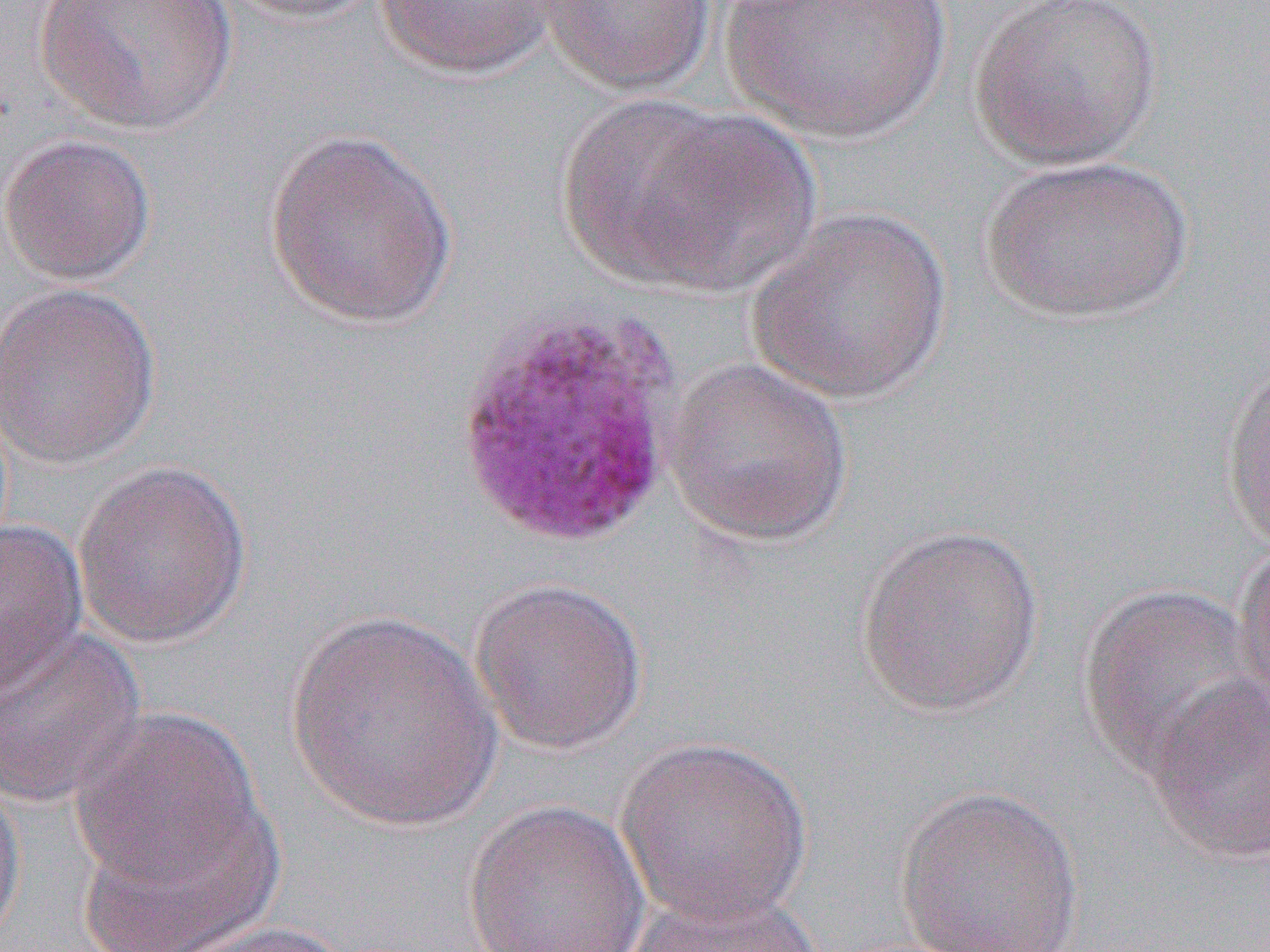
Approximate bounding boxes as (x1,y1)-(x2,y2) corner pairs in pixels. Uninfected red blood cell locations: (35,0)-(237,135), (219,0)-(389,24), (374,0)-(558,79), (533,0)-(716,95), (721,0)-(950,143), (965,0)-(1164,171), (556,96)-(737,285), (623,109)-(825,296), (263,129)-(458,330), (0,133)-(156,286), (977,154)-(1195,324), (747,206)-(954,404), (0,280)-(162,469), (662,357)-(854,546), (1221,360)-(1270,555), (71,458)-(252,649), (0,518)-(88,700), (854,522)-(1046,716), (1233,539)-(1270,728), (469,576)-(649,756), (1077,583)-(1264,780), (284,608)-(502,833), (0,623)-(147,811), (1143,674)-(1270,866), (68,706)-(269,892), (615,735)-(813,927), (0,769)-(26,951), (894,783)-(1087,952), (69,793)-(286,952), (462,800)-(651,952), (623,888)-(829,952), (162,919)-(359,952). Slide-level diagnosis: Plasmodium vivax. 1000x magnification. Thin blood film. Optical microscopy. One field of a larger specimen. Image is 1270×952 pixels.